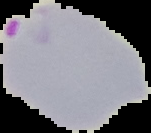

Summary:
  - Image type: segmented cell region with the area outside set to black
  - Preparation: thin blood smear
  - Malaria status: parasitized
  - Image size: 151×133 pixels